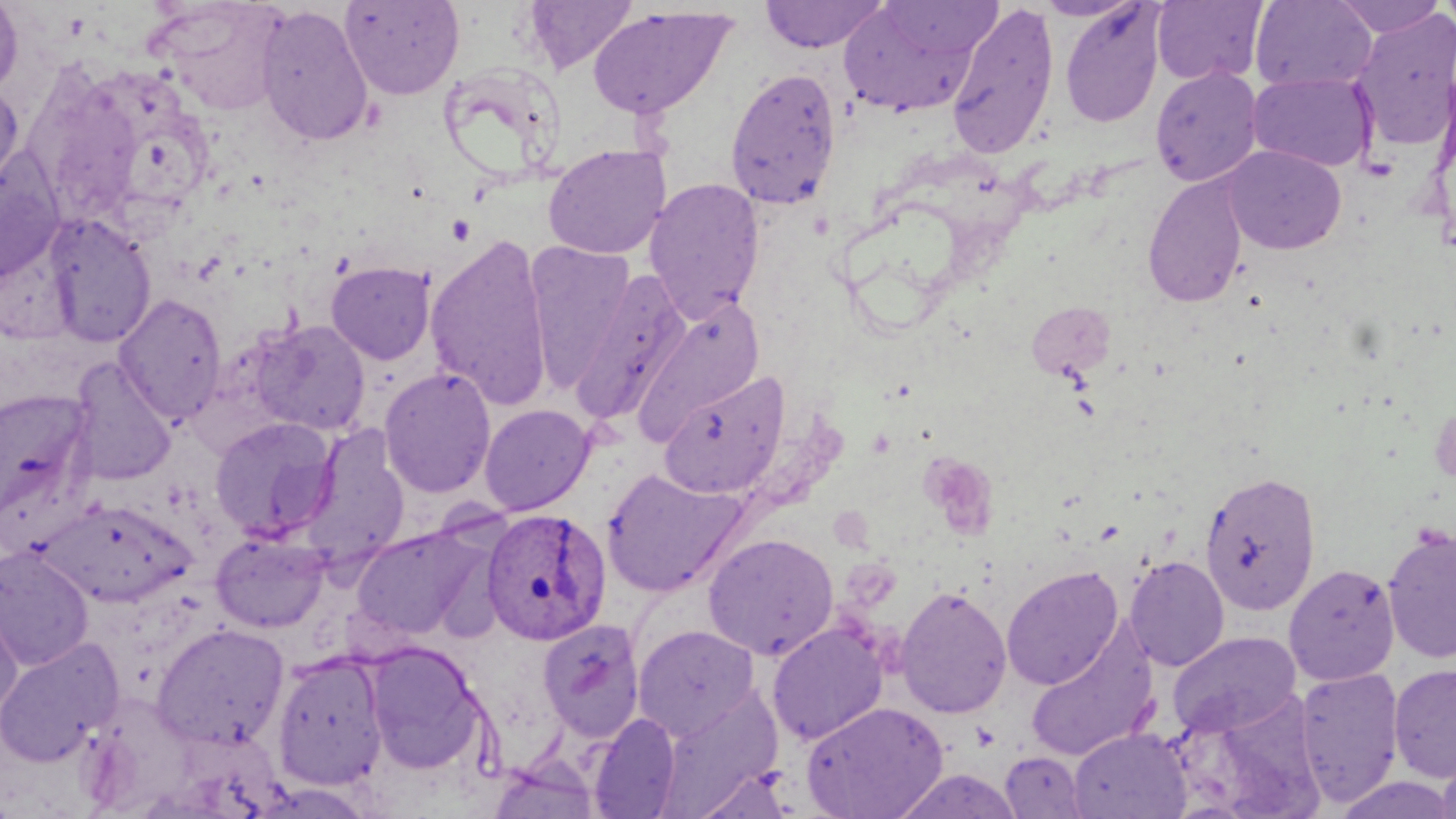

slide-level diagnosis = Plasmodium ovale
image size = 1456×819 pixels
modality = optical microscopy
field of view = one of a larger specimen
magnification = 1000x
stain = May-Grünwald-Giemsa
Plasmodium ovale-infected red blood cell locations = approximate bounding boxes as (x1, y1, x2, y2) in pixels: (481, 507, 612, 646)
preparation = thin blood film
uninfected red blood cell locations = approximate bounding boxes as (x1, y1, x2, y2) in pixels: (0, 0, 24, 98), (339, 0, 465, 101), (522, 0, 638, 74), (759, 0, 890, 53), (838, 0, 997, 117), (1035, 0, 1144, 21), (1332, 0, 1447, 38), (1438, 0, 1456, 31), (150, 1, 289, 115), (1152, 1, 1268, 85), (1251, 1, 1376, 92), (947, 2, 1058, 159), (1059, 3, 1165, 127), (255, 5, 373, 148), (587, 6, 736, 120), (1351, 10, 1456, 151), (439, 63, 563, 183), (1150, 64, 1264, 188), (21, 65, 150, 224), (725, 66, 842, 212), (1247, 71, 1376, 172), (0, 82, 25, 202), (542, 144, 671, 260), (1222, 145, 1347, 254), (0, 153, 65, 283), (1142, 174, 1249, 309), (643, 177, 765, 322), (43, 213, 157, 348), (425, 233, 555, 411), (523, 241, 636, 391), (325, 261, 436, 365), (568, 268, 694, 427), (113, 293, 227, 425), (633, 298, 766, 443), (1029, 301, 1114, 380), (250, 319, 370, 437), (67, 358, 177, 485), (378, 367, 497, 498), (658, 371, 789, 498), (0, 389, 95, 521), (479, 403, 595, 515), (209, 417, 339, 541), (300, 424, 410, 568), (602, 468, 746, 597), (1200, 470, 1321, 616), (42, 499, 196, 607), (1381, 524, 1456, 664), (350, 525, 488, 641), (211, 531, 330, 633), (702, 532, 840, 660), (0, 545, 95, 671), (1125, 555, 1230, 671), (1284, 563, 1400, 685), (1001, 566, 1123, 690), (895, 585, 1012, 719), (0, 590, 24, 720), (537, 618, 646, 744), (767, 621, 889, 745), (152, 622, 291, 750), (632, 624, 760, 740), (1026, 625, 1159, 762), (1168, 631, 1301, 738), (0, 637, 124, 767), (362, 640, 487, 774), (271, 651, 388, 792), (1388, 664, 1456, 781), (1294, 666, 1405, 807), (1177, 696, 1327, 817), (801, 700, 950, 818), (588, 712, 681, 818), (1069, 727, 1190, 818), (487, 751, 602, 819), (1000, 751, 1088, 818), (1436, 751, 1456, 819), (688, 766, 795, 818), (890, 768, 1023, 818), (1334, 773, 1456, 819)